Identify the preparation type.
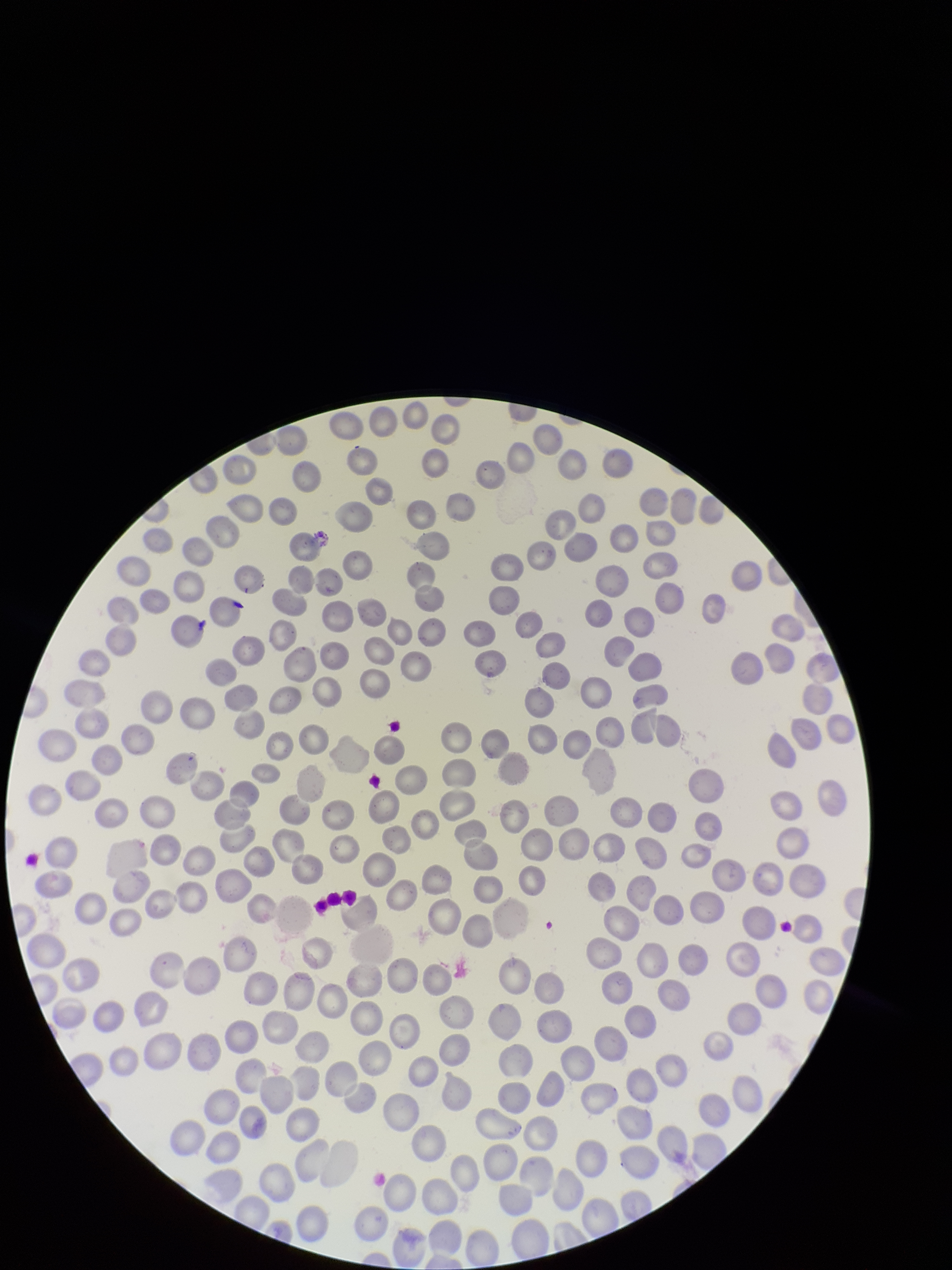

A thin smear.

image size = 952×1270 pixels
parasitized red blood cell count = 0
patient malaria status = infected
capture = smartphone photograph through the microscope eyepiece
parasitized red blood cells = none seen
stain = Giemsa
species reported for this patient = Plasmodium falciparum
red blood cell count = 263
field of view = one from this slide